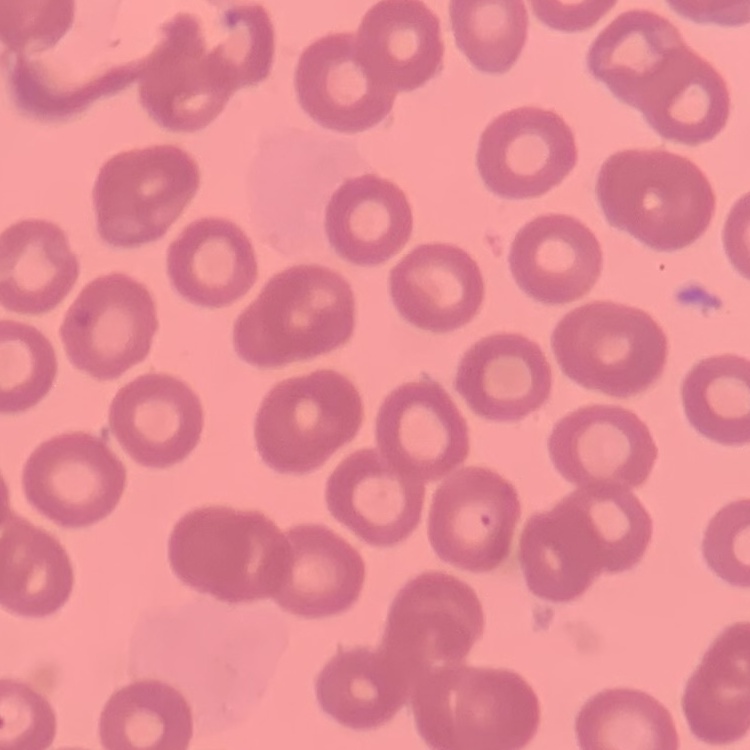

erythrocyte_morphology: no rouleaux formation
preparation: thin blood film
stain: Field's or Giemsa
image_type: one tile cut from a larger photomicrograph